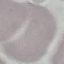 Result: no malaria parasites detected. Giemsa-stained preparation. Thin blood smear. Automatically extracted cell patch, resized to 64 × 64 pixels. Acquired by smartphone through the microscope eyepiece.